Locate every leukocyte (white blood cell).
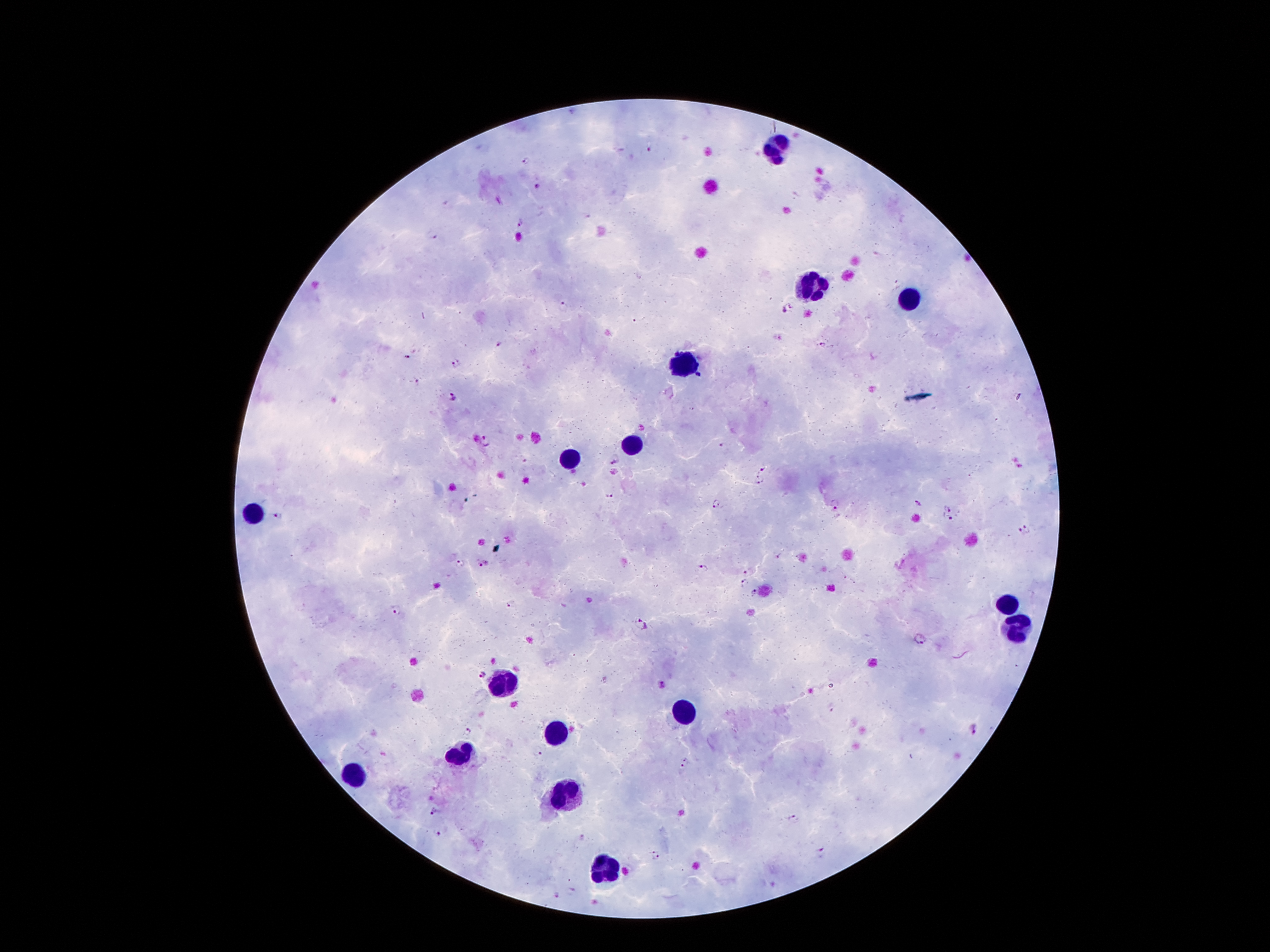

Approximate object centers, in pixels from the top-left corner.
Leukocytes: (x=774, y=148), (x=810, y=287), (x=906, y=298), (x=690, y=363), (x=634, y=441), (x=570, y=457), (x=253, y=510), (x=1009, y=602), (x=1016, y=627), (x=499, y=684), (x=682, y=709), (x=554, y=733), (x=461, y=754), (x=354, y=773), (x=570, y=794), (x=606, y=869).

Malaria parasite locations: (x=650, y=145), (x=527, y=161), (x=537, y=189), (x=520, y=224), (x=431, y=234), (x=563, y=305), (x=787, y=308), (x=634, y=321), (x=499, y=343), (x=822, y=343), (x=408, y=356), (x=455, y=364), (x=417, y=381), (x=453, y=397), (x=485, y=440), (x=723, y=445), (x=614, y=461), (x=763, y=469), (x=758, y=475), (x=760, y=484), (x=610, y=495), (x=916, y=503), (x=717, y=504), (x=833, y=505), (x=948, y=509), (x=281, y=516), (x=948, y=518), (x=1030, y=524), (x=1018, y=533), (x=460, y=563), (x=483, y=564), (x=704, y=569), (x=747, y=571), (x=746, y=581), (x=756, y=594), (x=512, y=605), (x=399, y=610), (x=641, y=622), (x=920, y=639), (x=832, y=710), (x=973, y=729), (x=468, y=732), (x=537, y=750), (x=685, y=763), (x=434, y=812), (x=794, y=819), (x=439, y=833), (x=582, y=838), (x=822, y=851), (x=656, y=855), (x=570, y=890), (x=556, y=896). Image is 1270×952 pixels. Giemsa stain. Single field of view. Thick blood smear. Smartphone photograph taken through the microscope eyepiece. 100x magnification. Patient malaria status: positive for Plasmodium falciparum.